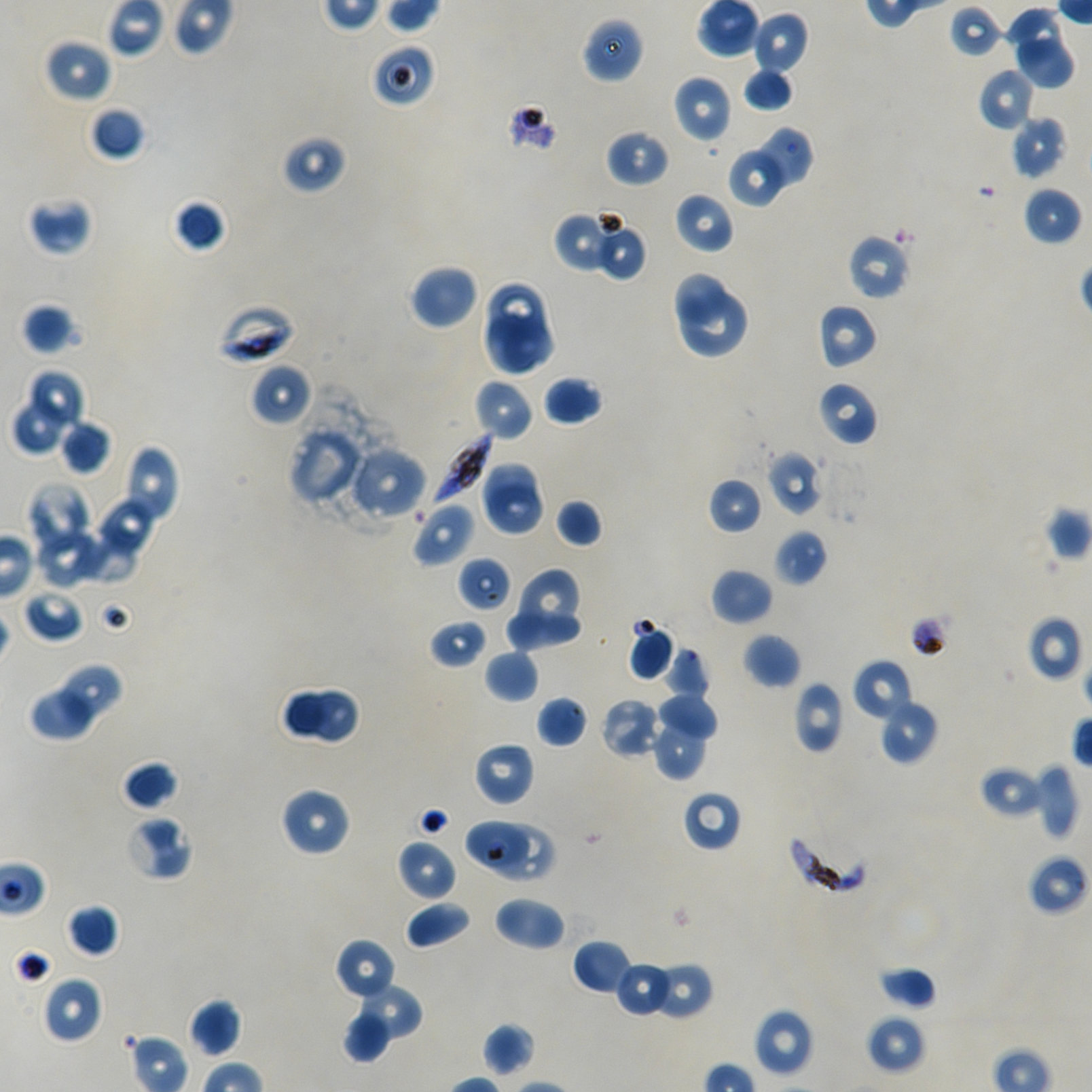
Approximate bounding rectangles given as corner coordinates in pixels from the top-left. Not every red blood cell is marked. Locations of red blood cells of indeterminate infection status: (x1=948, y1=4, x2=1005, y2=59), (x1=370, y1=41, x2=437, y2=108), (x1=457, y1=556, x2=513, y2=613), (x1=464, y1=818, x2=530, y2=872), (x1=498, y1=825, x2=551, y2=883). Locations of infected red blood cells: (x1=216, y1=302, x2=297, y2=365), (x1=429, y1=431, x2=492, y2=508), (x1=786, y1=829, x2=871, y2=896). Locations of uninfected red blood cells: (x1=1002, y1=5, x2=1064, y2=65), (x1=752, y1=12, x2=809, y2=77), (x1=581, y1=18, x2=644, y2=84), (x1=43, y1=37, x2=112, y2=103), (x1=1014, y1=40, x2=1076, y2=90), (x1=742, y1=67, x2=794, y2=113), (x1=977, y1=68, x2=1034, y2=132), (x1=672, y1=75, x2=731, y2=144), (x1=89, y1=107, x2=145, y2=161), (x1=1011, y1=115, x2=1068, y2=180), (x1=754, y1=126, x2=814, y2=184), (x1=605, y1=128, x2=670, y2=187), (x1=280, y1=134, x2=348, y2=195), (x1=727, y1=151, x2=784, y2=208), (x1=1021, y1=185, x2=1082, y2=247), (x1=673, y1=191, x2=735, y2=255), (x1=26, y1=193, x2=94, y2=256), (x1=172, y1=199, x2=226, y2=253), (x1=553, y1=213, x2=613, y2=273), (x1=592, y1=222, x2=647, y2=281), (x1=847, y1=234, x2=911, y2=301), (x1=410, y1=264, x2=479, y2=330), (x1=676, y1=270, x2=729, y2=327), (x1=484, y1=282, x2=547, y2=346), (x1=682, y1=293, x2=746, y2=357), (x1=21, y1=303, x2=80, y2=356), (x1=817, y1=303, x2=879, y2=369), (x1=481, y1=315, x2=556, y2=377), (x1=250, y1=363, x2=311, y2=426), (x1=31, y1=371, x2=84, y2=426), (x1=543, y1=375, x2=604, y2=426), (x1=473, y1=378, x2=534, y2=441), (x1=816, y1=380, x2=878, y2=446), (x1=11, y1=401, x2=62, y2=455), (x1=58, y1=419, x2=112, y2=475), (x1=288, y1=426, x2=366, y2=506), (x1=117, y1=445, x2=179, y2=534), (x1=347, y1=445, x2=427, y2=520), (x1=767, y1=450, x2=823, y2=516), (x1=477, y1=463, x2=535, y2=517), (x1=706, y1=477, x2=763, y2=534), (x1=26, y1=481, x2=95, y2=558), (x1=486, y1=484, x2=546, y2=539), (x1=96, y1=496, x2=158, y2=559), (x1=555, y1=498, x2=603, y2=548), (x1=412, y1=501, x2=476, y2=567), (x1=75, y1=524, x2=132, y2=581), (x1=772, y1=528, x2=828, y2=587), (x1=35, y1=531, x2=106, y2=589), (x1=710, y1=568, x2=774, y2=625), (x1=520, y1=570, x2=578, y2=634), (x1=22, y1=587, x2=85, y2=643), (x1=506, y1=612, x2=583, y2=646), (x1=1025, y1=615, x2=1085, y2=682), (x1=429, y1=617, x2=488, y2=670), (x1=628, y1=621, x2=676, y2=681), (x1=742, y1=632, x2=801, y2=689), (x1=664, y1=645, x2=710, y2=699), (x1=484, y1=649, x2=541, y2=703), (x1=853, y1=658, x2=913, y2=721), (x1=62, y1=667, x2=121, y2=722), (x1=792, y1=681, x2=845, y2=754), (x1=33, y1=685, x2=96, y2=738), (x1=278, y1=685, x2=327, y2=743), (x1=310, y1=689, x2=361, y2=744), (x1=657, y1=692, x2=718, y2=742), (x1=536, y1=695, x2=589, y2=748), (x1=877, y1=697, x2=939, y2=765), (x1=600, y1=698, x2=661, y2=760), (x1=652, y1=716, x2=704, y2=781), (x1=473, y1=741, x2=535, y2=806), (x1=122, y1=760, x2=179, y2=811), (x1=1035, y1=761, x2=1080, y2=843), (x1=979, y1=765, x2=1044, y2=819), (x1=280, y1=786, x2=352, y2=858), (x1=681, y1=790, x2=742, y2=852), (x1=124, y1=813, x2=194, y2=880), (x1=397, y1=839, x2=458, y2=901), (x1=1027, y1=853, x2=1091, y2=915), (x1=492, y1=896, x2=566, y2=951), (x1=404, y1=900, x2=472, y2=949), (x1=66, y1=903, x2=118, y2=958), (x1=334, y1=938, x2=397, y2=1002), (x1=571, y1=940, x2=632, y2=995), (x1=614, y1=961, x2=673, y2=1018), (x1=649, y1=961, x2=713, y2=1020), (x1=877, y1=966, x2=936, y2=1010), (x1=41, y1=976, x2=103, y2=1044), (x1=362, y1=981, x2=422, y2=1041), (x1=187, y1=998, x2=242, y2=1057), (x1=753, y1=1007, x2=814, y2=1077), (x1=342, y1=1013, x2=389, y2=1060), (x1=866, y1=1014, x2=926, y2=1074), (x1=482, y1=1023, x2=536, y2=1077). Image is 1092×1092 pixels. Single field of view. Blood group of the donor: A+/O+. Thin blood film. Giemsa stain. Oil immersion, 100x objective (numerical aperture 1.45). P. falciparum strain NF54 in static in-vitro culture.